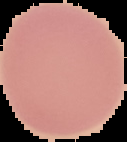

Image is 127×142 pixels. The area outside the segmented cell region is set to black. Result: no malaria parasites detected. From a thin blood film.